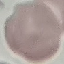

malaria_status: uninfected
capture: smartphone through the microscope eyepiece
stain: Giemsa
image_type: cell patch, automatically extracted from a larger field of view and resized to 64 × 64 pixels
preparation: thin blood film